Give the position of every Plasmodium parasite visible.
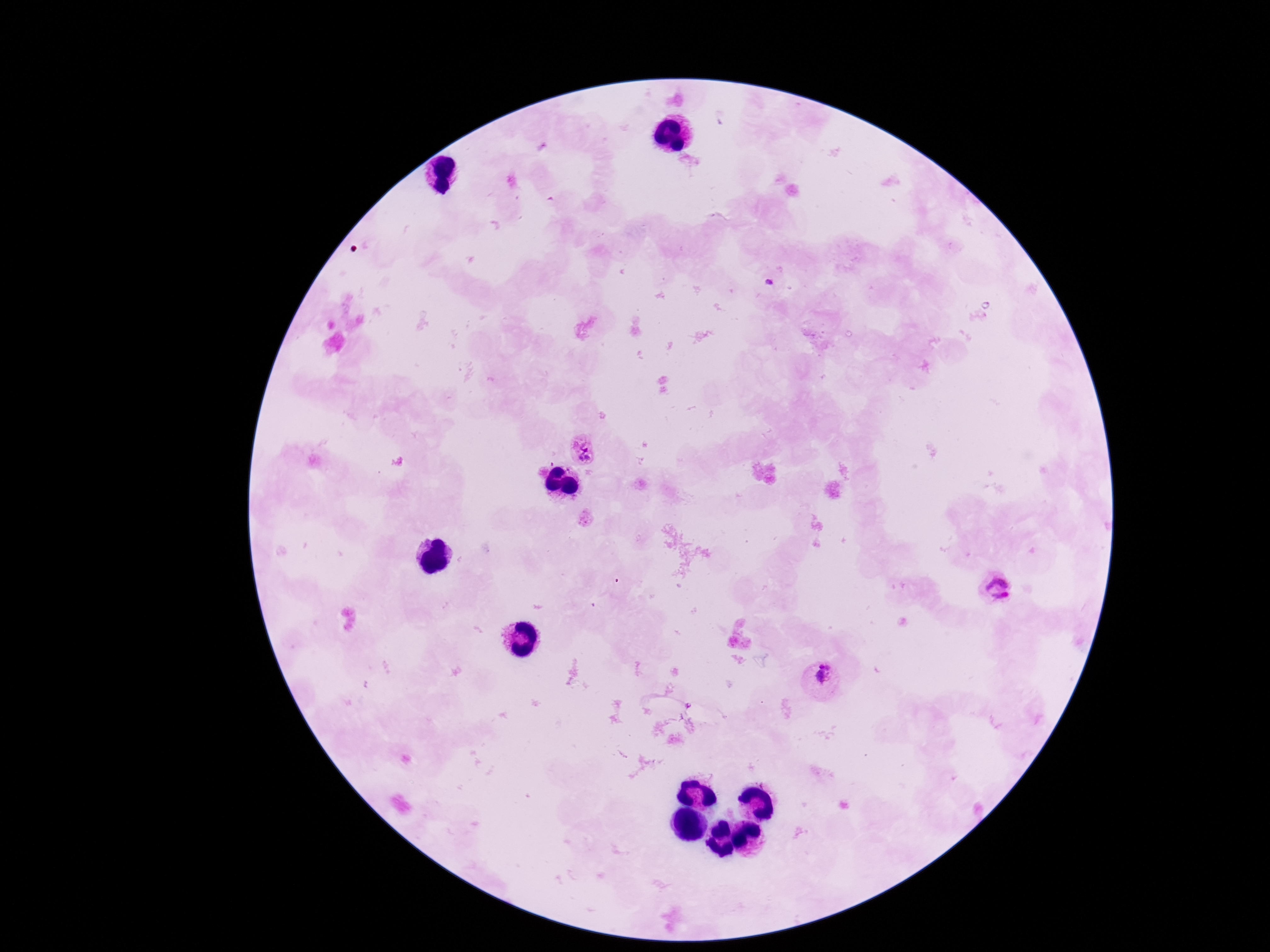

Approximate object centers, in pixels from the top-left corner.
Plasmodium parasites: (x=581, y=447), (x=998, y=594), (x=821, y=680).

Thick blood film. Giemsa stain. Single field of view. Image is 1270×952 pixels. Photographed through the microscope eyepiece with a smartphone camera. 100x magnification. Patient malaria status: infected.